Assess this cell for malaria.
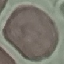

Uninfected.

preparation = thin smear
capture = smartphone through the microscope eyepiece
image type = cell patch, automatically extracted from a larger field of view and resized to 64 × 64 pixels
stain = Giemsa